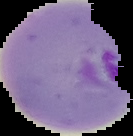

image type = segmented cell region on a black background
result = Plasmodium parasites identified
preparation = thin blood smear
image size = 133×136 pixels